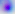
identification = Toxoplasma gondii
modality = micrograph
magnification = 400x